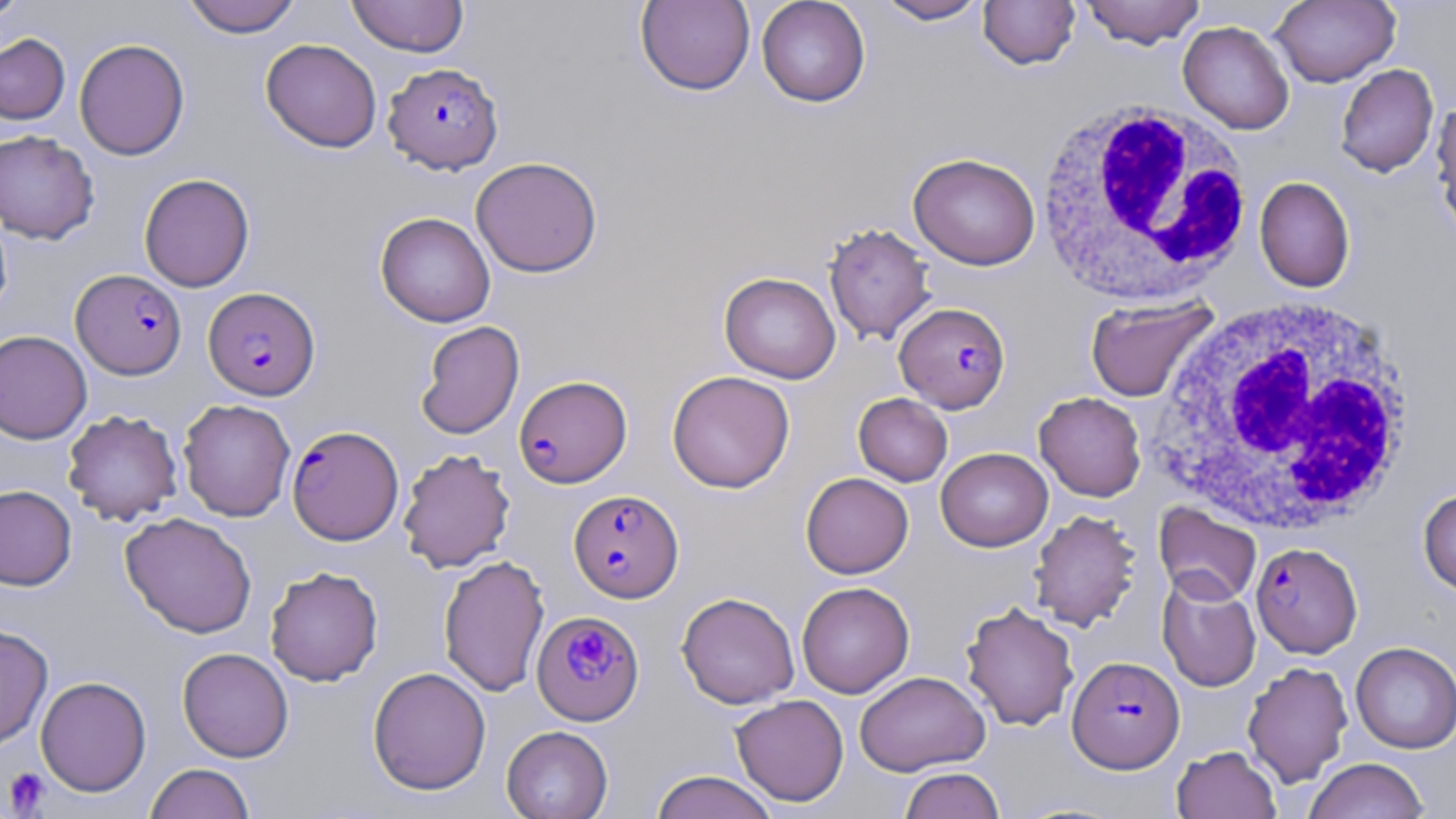
{
  "slide_level_diagnosis": "Plasmodium falciparum",
  "field_of_view": "single",
  "magnification": "1000x",
  "white_blood_cell_locations": "approximate bounding boxes as named x1/y1/x2/y2 corners in pixels: (x1=1033, y1=98, x2=1256, y2=308), (x1=1148, y1=296, x2=1419, y2=535)",
  "platelet_locations": "approximate bounding boxes as named x1/y1/x2/y2 corners in pixels: (x1=2, y1=766, x2=52, y2=817)",
  "stain": "May-Grünwald-Giemsa",
  "image_size": "1456×819 pixels",
  "preparation": "thin blood smear",
  "uninfected_red_blood_cell_locations": "approximate bounding boxes as named x1/y1/x2/y2 corners in pixels: (x1=0, y1=0, x2=29, y2=22), (x1=181, y1=0, x2=302, y2=37), (x1=346, y1=0, x2=469, y2=57), (x1=756, y1=0, x2=871, y2=107), (x1=874, y1=0, x2=991, y2=25), (x1=978, y1=0, x2=1081, y2=70), (x1=1078, y1=0, x2=1206, y2=49), (x1=1270, y1=0, x2=1400, y2=88), (x1=635, y1=1, x2=755, y2=96), (x1=1178, y1=21, x2=1294, y2=134), (x1=0, y1=33, x2=70, y2=125), (x1=74, y1=38, x2=190, y2=160), (x1=261, y1=38, x2=382, y2=153), (x1=1335, y1=63, x2=1439, y2=177), (x1=1432, y1=97, x2=1456, y2=240), (x1=0, y1=130, x2=99, y2=245), (x1=908, y1=152, x2=1040, y2=269), (x1=470, y1=156, x2=602, y2=277), (x1=139, y1=173, x2=255, y2=292), (x1=1254, y1=176, x2=1355, y2=292), (x1=0, y1=205, x2=13, y2=320), (x1=375, y1=212, x2=495, y2=327), (x1=823, y1=222, x2=936, y2=345), (x1=719, y1=272, x2=841, y2=384), (x1=1083, y1=296, x2=1219, y2=404), (x1=415, y1=320, x2=524, y2=440), (x1=0, y1=330, x2=92, y2=444), (x1=667, y1=370, x2=795, y2=493), (x1=1034, y1=391, x2=1146, y2=501), (x1=853, y1=393, x2=953, y2=486), (x1=178, y1=399, x2=295, y2=521), (x1=62, y1=409, x2=183, y2=526), (x1=936, y1=447, x2=1053, y2=552), (x1=398, y1=448, x2=516, y2=573), (x1=801, y1=472, x2=913, y2=578), (x1=0, y1=484, x2=77, y2=590), (x1=1418, y1=489, x2=1456, y2=597), (x1=1153, y1=502, x2=1262, y2=606), (x1=1028, y1=509, x2=1142, y2=631), (x1=120, y1=511, x2=257, y2=638), (x1=438, y1=554, x2=549, y2=697), (x1=264, y1=566, x2=383, y2=686), (x1=1157, y1=574, x2=1261, y2=691), (x1=796, y1=581, x2=914, y2=698), (x1=677, y1=592, x2=800, y2=708), (x1=960, y1=601, x2=1079, y2=731), (x1=0, y1=624, x2=53, y2=752), (x1=1350, y1=641, x2=1456, y2=753), (x1=177, y1=647, x2=294, y2=762), (x1=1242, y1=660, x2=1353, y2=787), (x1=368, y1=666, x2=491, y2=795), (x1=854, y1=670, x2=990, y2=776), (x1=35, y1=675, x2=151, y2=796), (x1=730, y1=694, x2=849, y2=807), (x1=501, y1=725, x2=613, y2=819), (x1=1172, y1=745, x2=1281, y2=819), (x1=1304, y1=757, x2=1430, y2=819), (x1=145, y1=763, x2=255, y2=819), (x1=899, y1=767, x2=1005, y2=818), (x1=649, y1=770, x2=779, y2=819)",
  "plasmodium_falciparum_infected_red_blood_cell_locations": "approximate bounding boxes as named x1/y1/x2/y2 corners in pixels: (x1=383, y1=61, x2=504, y2=174), (x1=71, y1=269, x2=186, y2=379), (x1=203, y1=286, x2=320, y2=400), (x1=895, y1=302, x2=1011, y2=413), (x1=513, y1=375, x2=632, y2=488), (x1=287, y1=425, x2=403, y2=545), (x1=569, y1=489, x2=684, y2=602), (x1=1251, y1=542, x2=1362, y2=657), (x1=532, y1=611, x2=644, y2=726), (x1=1068, y1=656, x2=1184, y2=773)",
  "modality": "light microscopy"
}